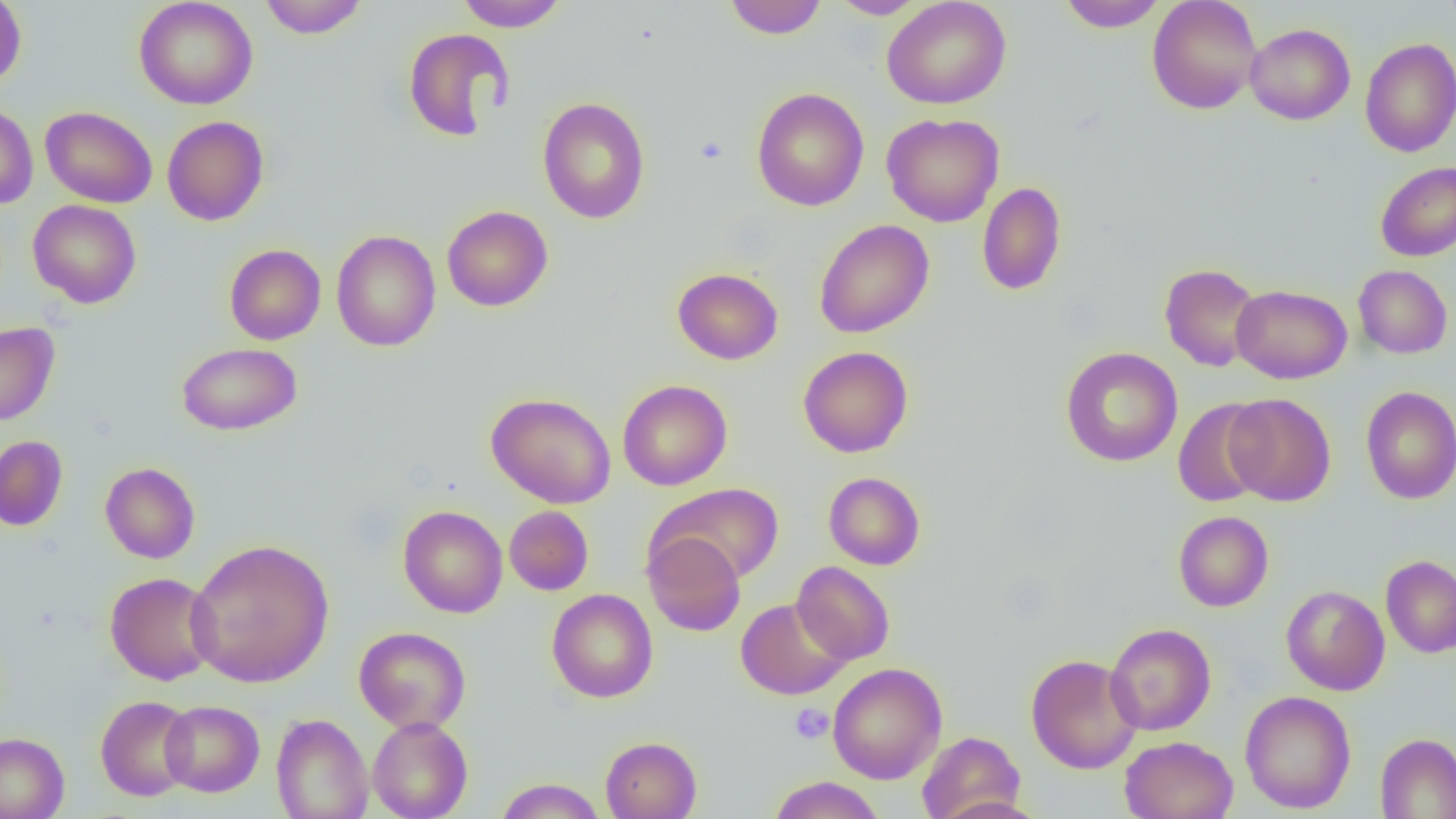
slide-level diagnosis = no evidence of blood parasites
image size = 1456×819 pixels
magnification = 1000x
uninfected red blood cell locations = approximate bounding boxes as named x1/y1/x2/y2 corners in pixels: (x1=0, y1=0, x2=26, y2=88), (x1=134, y1=0, x2=259, y2=110), (x1=259, y1=0, x2=368, y2=38), (x1=455, y1=0, x2=567, y2=31), (x1=723, y1=0, x2=827, y2=39), (x1=829, y1=0, x2=928, y2=19), (x1=881, y1=0, x2=1012, y2=109), (x1=1057, y1=0, x2=1168, y2=31), (x1=1147, y1=0, x2=1262, y2=115), (x1=1245, y1=23, x2=1355, y2=125), (x1=402, y1=27, x2=514, y2=141), (x1=1360, y1=37, x2=1456, y2=157), (x1=751, y1=87, x2=869, y2=211), (x1=537, y1=97, x2=651, y2=224), (x1=0, y1=103, x2=38, y2=210), (x1=40, y1=106, x2=157, y2=208), (x1=881, y1=113, x2=1005, y2=227), (x1=162, y1=116, x2=269, y2=226), (x1=1375, y1=161, x2=1456, y2=261), (x1=976, y1=181, x2=1067, y2=296), (x1=28, y1=200, x2=142, y2=309), (x1=442, y1=205, x2=553, y2=312), (x1=813, y1=219, x2=934, y2=338), (x1=331, y1=230, x2=441, y2=352), (x1=224, y1=244, x2=325, y2=345), (x1=1159, y1=263, x2=1264, y2=372), (x1=1353, y1=265, x2=1452, y2=359), (x1=672, y1=268, x2=783, y2=365), (x1=1231, y1=284, x2=1352, y2=384), (x1=0, y1=322, x2=60, y2=426), (x1=176, y1=342, x2=301, y2=436), (x1=798, y1=346, x2=913, y2=458), (x1=1061, y1=347, x2=1183, y2=467), (x1=617, y1=379, x2=732, y2=491), (x1=1360, y1=386, x2=1456, y2=504), (x1=485, y1=392, x2=616, y2=508), (x1=1225, y1=393, x2=1336, y2=506), (x1=1172, y1=398, x2=1271, y2=507), (x1=0, y1=436, x2=68, y2=531), (x1=100, y1=462, x2=200, y2=564), (x1=823, y1=472, x2=926, y2=570), (x1=652, y1=483, x2=785, y2=584), (x1=398, y1=504, x2=508, y2=618), (x1=504, y1=506, x2=594, y2=596), (x1=1173, y1=511, x2=1273, y2=612), (x1=643, y1=531, x2=746, y2=636), (x1=185, y1=538, x2=335, y2=688), (x1=1381, y1=555, x2=1456, y2=658), (x1=792, y1=561, x2=894, y2=665), (x1=105, y1=572, x2=218, y2=686), (x1=1281, y1=585, x2=1390, y2=696), (x1=546, y1=589, x2=658, y2=703), (x1=735, y1=597, x2=850, y2=700), (x1=1105, y1=623, x2=1216, y2=735), (x1=353, y1=626, x2=471, y2=733), (x1=1025, y1=653, x2=1143, y2=774), (x1=827, y1=662, x2=947, y2=784), (x1=1240, y1=690, x2=1356, y2=813), (x1=95, y1=695, x2=197, y2=801), (x1=160, y1=700, x2=264, y2=796), (x1=160, y1=707, x2=373, y2=803), (x1=271, y1=713, x2=373, y2=819), (x1=367, y1=716, x2=473, y2=819), (x1=916, y1=730, x2=1026, y2=819), (x1=0, y1=732, x2=69, y2=819), (x1=1375, y1=732, x2=1456, y2=819), (x1=600, y1=736, x2=702, y2=819), (x1=1119, y1=736, x2=1238, y2=819), (x1=768, y1=776, x2=886, y2=819), (x1=494, y1=778, x2=607, y2=818)
preparation = thin blood smear
platelet locations = approximate bounding boxes as named x1/y1/x2/y2 corners in pixels: (x1=695, y1=136, x2=727, y2=165), (x1=789, y1=703, x2=832, y2=743)
field of view = single
modality = optical microscopy